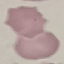
Summary:
  - Result: no malaria parasites seen
  - Capture: smartphone camera at the microscope eyepiece
  - Preparation: thin blood smear
  - Stain: Giemsa
  - Image type: automatically extracted cell patch, resized to 64 × 64 pixels